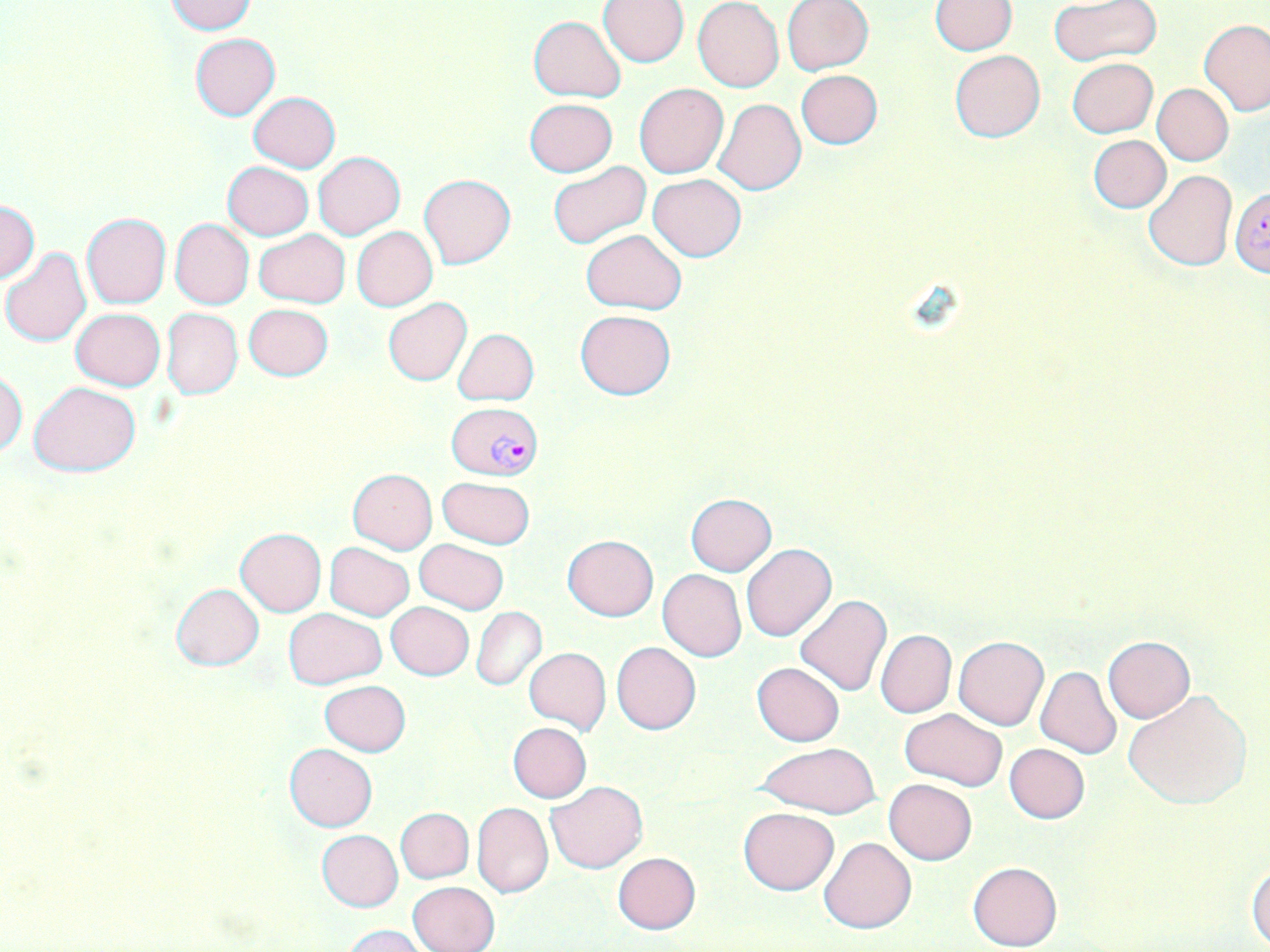
Approximate bounding boxes as (x1,y1)-(x2,y2) corner pairs in pixels. Uninfected red blood cell locations: (164,0)-(256,34), (783,0)-(874,74), (930,0)-(1018,54), (598,1)-(690,66), (692,1)-(784,92), (1047,2)-(1161,66), (529,16)-(626,101), (1199,18)-(1270,115), (190,33)-(280,120), (949,49)-(1044,142), (1067,57)-(1157,137), (795,70)-(883,150), (635,83)-(728,178), (1153,84)-(1234,165), (247,91)-(341,172), (713,97)-(807,195), (524,98)-(618,177), (1089,135)-(1171,213), (312,150)-(405,239), (222,161)-(314,241), (548,161)-(650,249), (1143,171)-(1237,270), (418,174)-(516,269), (647,174)-(746,262), (0,200)-(40,283), (81,212)-(172,309), (170,218)-(254,309), (352,226)-(437,311), (255,229)-(350,308), (581,230)-(686,314), (0,247)-(91,348), (382,298)-(471,386), (244,303)-(333,380), (70,308)-(165,391), (161,308)-(242,399), (574,309)-(676,400), (453,328)-(538,405), (0,366)-(26,457), (28,381)-(142,476), (348,468)-(436,554), (437,475)-(535,549), (686,494)-(778,576), (234,528)-(327,615), (562,535)-(658,619), (415,538)-(509,613), (324,542)-(414,620), (741,544)-(836,642), (658,569)-(747,660), (171,583)-(265,671), (794,595)-(893,698), (386,601)-(474,680), (472,607)-(546,691), (284,608)-(386,689), (876,629)-(956,718), (1103,635)-(1194,722), (954,636)-(1048,730), (611,642)-(700,735), (523,648)-(611,737), (751,661)-(844,746), (1036,666)-(1122,758), (319,680)-(411,756), (1123,690)-(1252,810), (901,709)-(1006,791), (508,722)-(591,803), (756,742)-(881,819), (1005,743)-(1089,824), (284,745)-(377,831), (884,779)-(976,865), (546,781)-(648,873), (471,803)-(553,898), (395,807)-(473,883), (738,807)-(839,895), (317,830)-(403,911), (820,837)-(915,933), (612,852)-(701,933), (967,861)-(1061,950), (1248,862)-(1270,947), (408,882)-(500,951), (343,925)-(427,952). Plasmodium falciparum-infected red blood cell locations: (1229,189)-(1270,276), (449,400)-(537,479). Slide-level diagnosis: Plasmodium falciparum. One field of a larger specimen. Thin blood smear. May-Grünwald-Giemsa stain. Image is 1270×952 pixels. Light microscopy. Captured at 1000x magnification.